State which cell type is depicted.
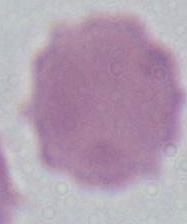

This is an erythrocyte.

Captured at 1000x magnification. Photomicrograph.